Describe the morphology of the erythrocytes.
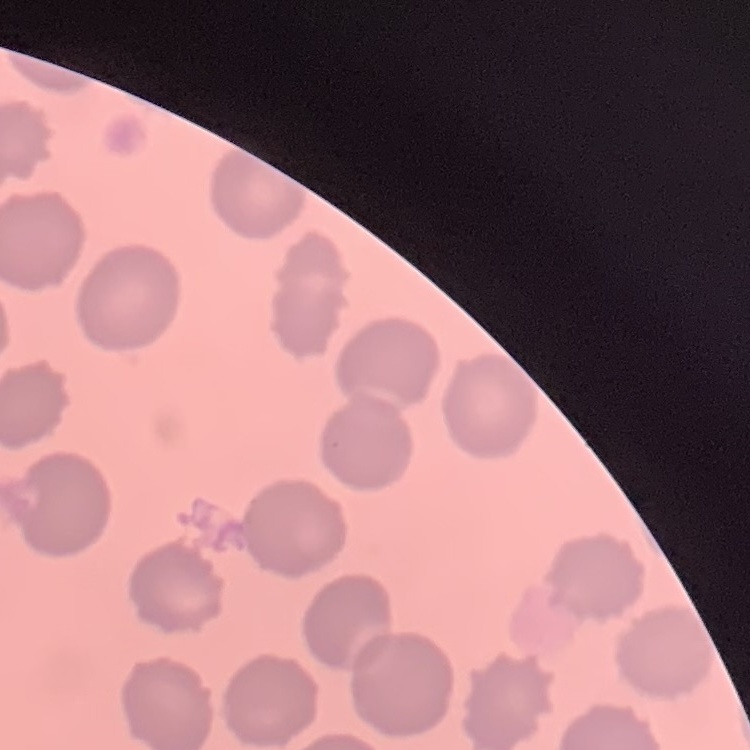

No rouleaux formation.

stain = Field's or Giemsa
image type = one tile cut from a larger photomicrograph
preparation = thin blood film